State which parasite is depicted.
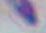
Toxoplasma gondii.

Summary:
  - Modality: micrograph
  - Magnification: 1000x